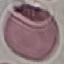
result = negative for malaria parasites
image type = automatically extracted cell patch, resized to 64 × 64 pixels
stain = Giemsa
preparation = thin smear
capture = smartphone camera at the microscope eyepiece